Name the blood parasite species.
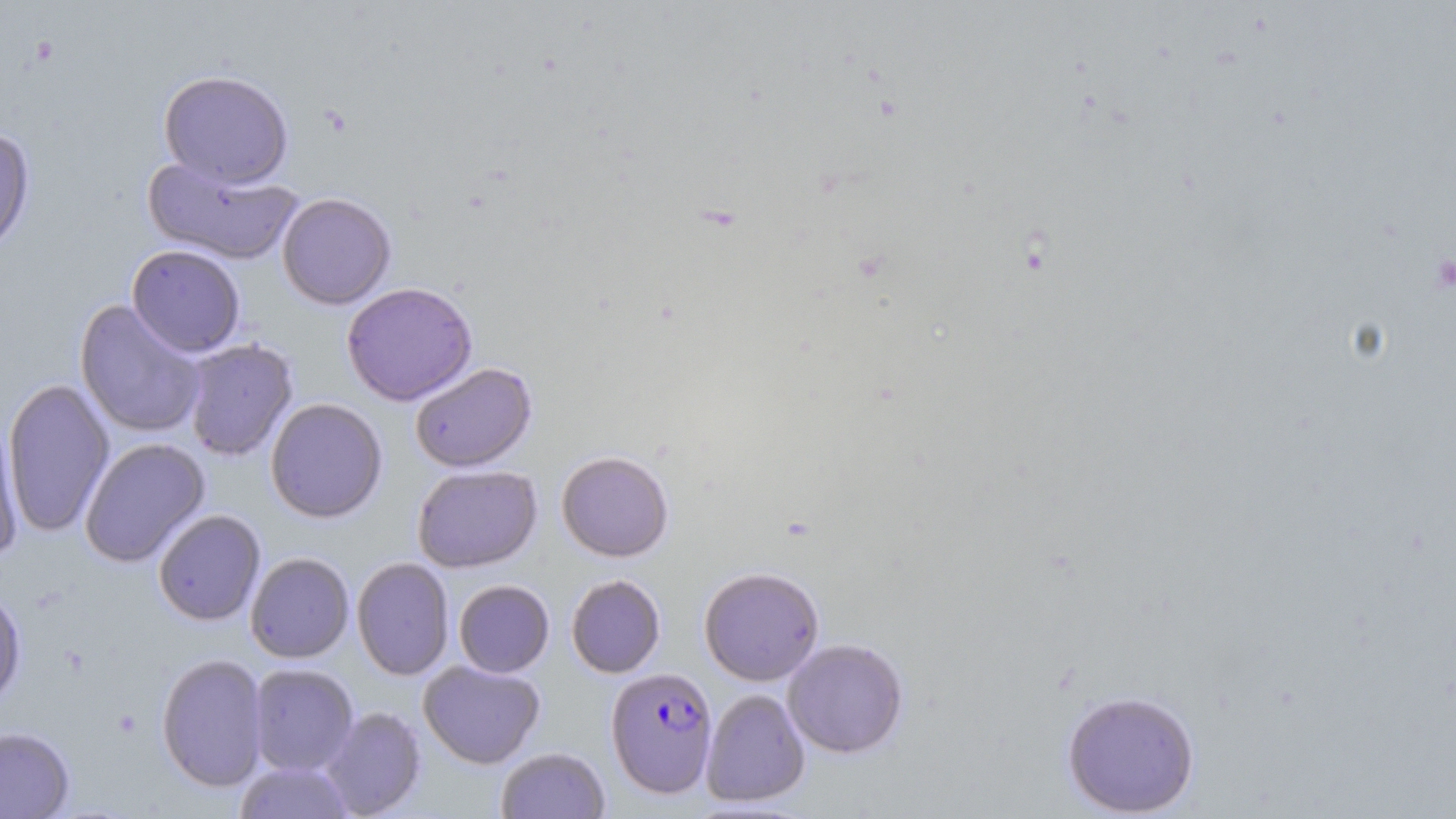

Plasmodium falciparum.

Summary:
  - Coordinate format: approximate bounding boxes as named x1/y1/x2/y2 corners in pixels
  - Platelet locations: (x1=1432, y1=255, x2=1456, y2=292)
  - Plasmodium falciparum-infected red blood cell locations: (x1=605, y1=666, x2=718, y2=798)
  - Uninfected red blood cell locations: (x1=157, y1=69, x2=294, y2=189), (x1=0, y1=125, x2=35, y2=257), (x1=142, y1=155, x2=303, y2=266), (x1=277, y1=192, x2=396, y2=310), (x1=126, y1=244, x2=246, y2=357), (x1=341, y1=282, x2=478, y2=406), (x1=75, y1=300, x2=207, y2=438), (x1=184, y1=339, x2=298, y2=461), (x1=410, y1=362, x2=537, y2=473), (x1=3, y1=378, x2=115, y2=537), (x1=265, y1=398, x2=388, y2=523), (x1=0, y1=414, x2=26, y2=562), (x1=80, y1=438, x2=210, y2=567), (x1=556, y1=450, x2=674, y2=562), (x1=412, y1=464, x2=542, y2=573), (x1=153, y1=509, x2=266, y2=626), (x1=245, y1=552, x2=354, y2=663), (x1=352, y1=557, x2=455, y2=680), (x1=698, y1=566, x2=824, y2=686), (x1=566, y1=574, x2=666, y2=678), (x1=453, y1=580, x2=554, y2=677), (x1=0, y1=585, x2=26, y2=710), (x1=782, y1=637, x2=909, y2=758), (x1=156, y1=652, x2=269, y2=793), (x1=418, y1=660, x2=545, y2=769), (x1=248, y1=663, x2=358, y2=775), (x1=700, y1=688, x2=811, y2=807), (x1=1061, y1=689, x2=1200, y2=817), (x1=320, y1=706, x2=426, y2=818), (x1=0, y1=726, x2=75, y2=818), (x1=496, y1=747, x2=610, y2=819), (x1=234, y1=760, x2=355, y2=819)
  - Stain: May-Grünwald-Giemsa
  - Preparation: thin blood film
  - Image size: 1456×819 pixels
  - Modality: optical microscopy
  - Magnification: 1000x
  - Field of view: one of a larger specimen